Name the blood parasite species.
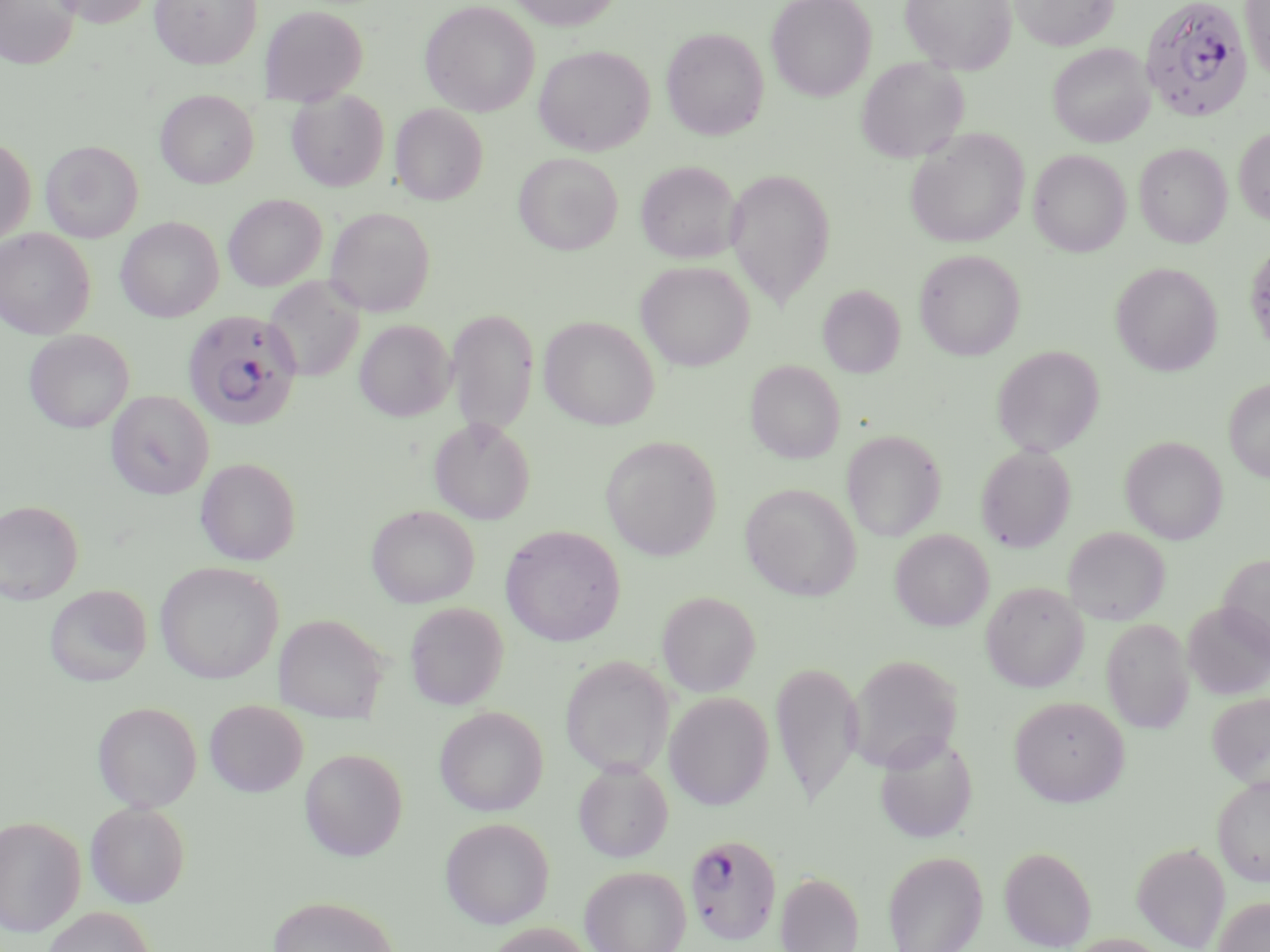
Plasmodium falciparum.

field_of_view: single
image_size: 1270×952 pixels
preparation: thin blood film
modality: light microscopy
magnification: 1000x
uninfected_red_blood_cell_locations: 'approximate bounding boxes as (x1,y1)-(x2,y2) corner pairs in pixels: (0,0)-(80,68), (47,0)-(155,27), (149,0)-(262,68), (506,0)-(622,30), (766,0)-(877,102), (899,0)-(1017,74), (1010,0)-(1118,51), (1239,0)-(1270,83), (420,1)-(540,117), (260,5)-(368,104), (661,27)-(769,140), (1048,43)-(1154,147), (534,44)-(654,156), (856,56)-(968,163), (287,90)-(389,191), (156,91)-(258,188), (390,103)-(488,205), (1234,126)-(1270,226), (905,129)-(1029,248), (0,137)-(35,247), (40,140)-(143,243), (1134,143)-(1232,248), (1028,149)-(1131,257), (513,152)-(622,255), (635,160)-(742,263), (725,168)-(835,309), (223,194)-(327,291), (325,206)-(436,316), (116,217)-(224,321), (0,228)-(95,338), (913,249)-(1025,360), (635,260)-(754,371), (1111,262)-(1222,376), (263,277)-(364,383), (817,285)-(905,378), (446,308)-(539,436), (539,316)-(659,430), (354,319)-(455,421), (24,330)-(134,433), (991,345)-(1105,456), (745,360)-(845,464), (1223,378)-(1270,482), (106,390)-(214,499), (429,418)-(535,525), (842,430)-(947,541), (601,436)-(721,561), (1120,436)-(1227,544), (976,445)-(1076,552), (196,458)-(301,566), (740,482)-(861,600), (0,500)-(84,604), (366,505)-(479,608), (499,524)-(626,647), (1063,527)-(1171,625), (890,529)-(994,631), (1217,553)-(1270,659), (155,561)-(283,684), (981,581)-(1089,692), (44,585)-(152,687), (657,591)-(760,697), (405,602)-(508,710), (1182,602)-(1269,700), (276,613)-(388,723), (1102,618)-(1194,734), (847,654)-(963,772), (560,656)-(675,778), (771,659)-(864,809), (664,692)-(774,810), (1207,692)-(1270,789), (1009,695)-(1130,806), (204,700)-(307,797), (93,701)-(202,812), (434,706)-(548,816), (874,731)-(978,843), (299,748)-(408,861), (573,760)-(673,862), (1212,775)-(1270,886), (85,801)-(190,907), (0,816)-(85,936), (440,817)-(554,929), (1131,843)-(1230,951), (999,846)-(1096,951), (882,850)-(988,952), (580,865)-(691,952), (775,871)-(864,952), (267,895)-(400,952), (1213,896)-(1270,952), (40,906)-(156,952), (484,922)-(595,952), (1063,934)-(1173,952)'
plasmodium_falciparum_infected_red_blood_cell_locations: 'approximate bounding boxes as (x1,y1)-(x2,y2) corner pairs in pixels: (1139,0)-(1252,122), (182,310)-(302,430), (685,832)-(782,946)'
stain: May-Grünwald-Giemsa